Outline each Plasmodium malariae-infected red blood cell.
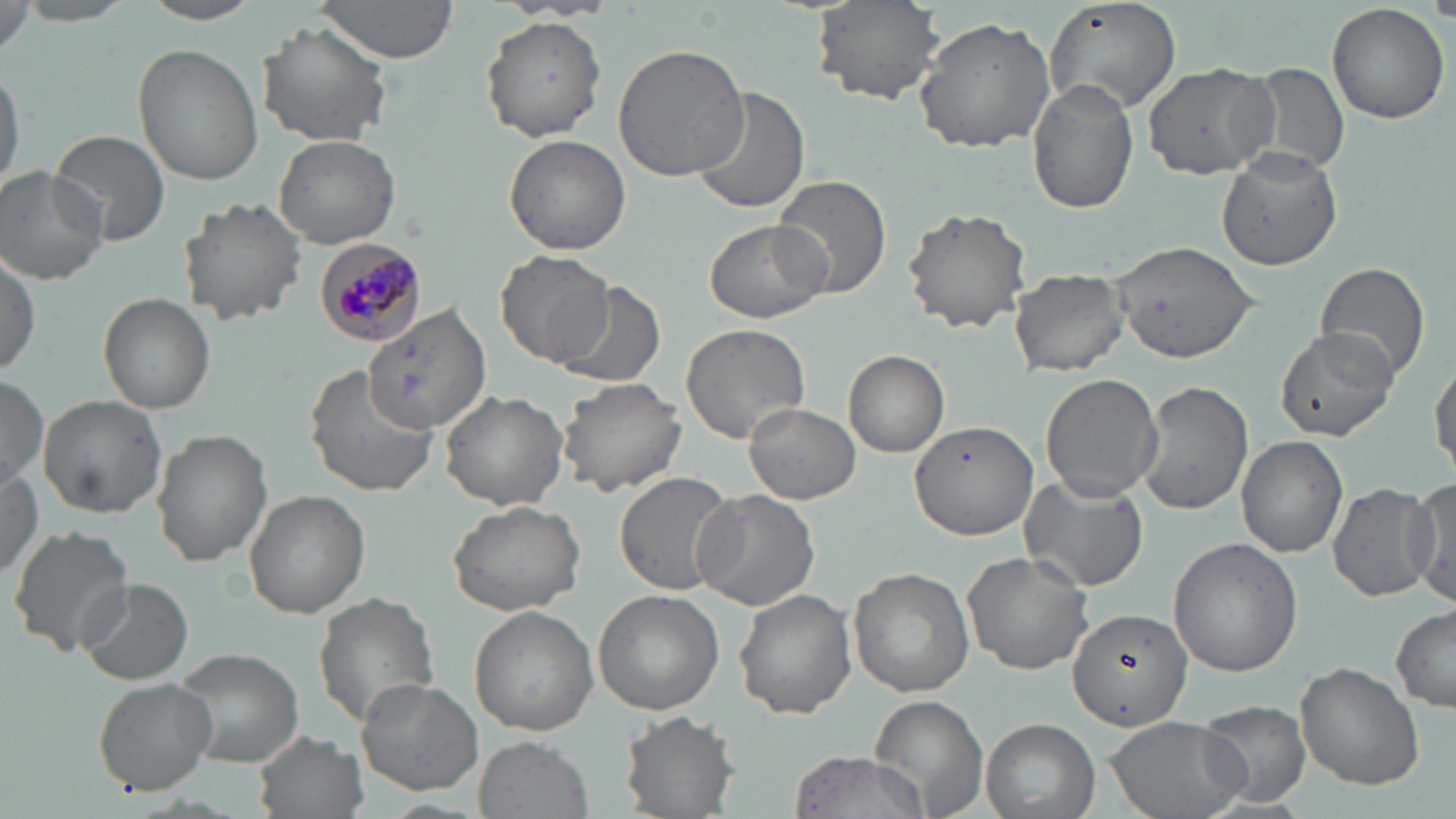

Approximate bounding boxes as named x1/y1/x2/y2 corners in pixels.
Plasmodium malariae-infected red blood cells: (x1=314, y1=239, x2=425, y2=348).

slide-level diagnosis = Plasmodium malariae
magnification = 1000x
image size = 1456×819 pixels
stain = May-Grünwald-Giemsa
preparation = thin blood film
field of view = one of a larger specimen
modality = optical microscopy
uninfected red blood cell locations = approximate bounding boxes as named x1/y1/x2/y2 corners in pixels: (x1=314, y1=0, x2=460, y2=64), (x1=810, y1=0, x2=946, y2=107), (x1=1045, y1=0, x2=1182, y2=115), (x1=136, y1=1, x2=266, y2=25), (x1=1326, y1=4, x2=1450, y2=125), (x1=480, y1=16, x2=607, y2=140), (x1=913, y1=16, x2=1058, y2=153), (x1=257, y1=21, x2=392, y2=147), (x1=613, y1=43, x2=754, y2=182), (x1=132, y1=44, x2=263, y2=185), (x1=0, y1=60, x2=24, y2=198), (x1=1142, y1=63, x2=1280, y2=181), (x1=1248, y1=63, x2=1350, y2=177), (x1=1028, y1=77, x2=1139, y2=214), (x1=688, y1=87, x2=811, y2=217), (x1=49, y1=129, x2=172, y2=244), (x1=274, y1=134, x2=401, y2=249), (x1=504, y1=135, x2=631, y2=255), (x1=1216, y1=147, x2=1345, y2=273), (x1=0, y1=167, x2=110, y2=286), (x1=773, y1=175, x2=893, y2=299), (x1=179, y1=198, x2=307, y2=324), (x1=901, y1=207, x2=1034, y2=333), (x1=703, y1=218, x2=834, y2=324), (x1=1114, y1=240, x2=1258, y2=362), (x1=1, y1=249, x2=42, y2=377), (x1=498, y1=250, x2=616, y2=369), (x1=1315, y1=261, x2=1431, y2=383), (x1=1008, y1=267, x2=1130, y2=377), (x1=553, y1=281, x2=669, y2=389), (x1=99, y1=292, x2=214, y2=414), (x1=362, y1=299, x2=492, y2=438), (x1=681, y1=322, x2=812, y2=443), (x1=1274, y1=327, x2=1396, y2=440), (x1=844, y1=351, x2=950, y2=457), (x1=1431, y1=351, x2=1456, y2=482), (x1=303, y1=366, x2=443, y2=500), (x1=1040, y1=373, x2=1163, y2=503), (x1=0, y1=375, x2=48, y2=487), (x1=555, y1=377, x2=687, y2=498), (x1=1136, y1=381, x2=1253, y2=515), (x1=440, y1=388, x2=569, y2=511), (x1=38, y1=394, x2=166, y2=518), (x1=744, y1=403, x2=860, y2=505), (x1=909, y1=421, x2=1036, y2=540), (x1=151, y1=427, x2=271, y2=565), (x1=1237, y1=435, x2=1348, y2=557), (x1=0, y1=463, x2=46, y2=582), (x1=613, y1=471, x2=736, y2=597), (x1=1018, y1=473, x2=1151, y2=591), (x1=1405, y1=479, x2=1456, y2=606), (x1=1327, y1=481, x2=1442, y2=603), (x1=690, y1=488, x2=819, y2=611), (x1=244, y1=489, x2=369, y2=617), (x1=446, y1=498, x2=587, y2=617), (x1=7, y1=526, x2=133, y2=657), (x1=1167, y1=536, x2=1303, y2=676), (x1=962, y1=551, x2=1098, y2=677), (x1=848, y1=568, x2=974, y2=697), (x1=77, y1=578, x2=194, y2=685), (x1=734, y1=588, x2=856, y2=718), (x1=311, y1=590, x2=442, y2=730), (x1=594, y1=591, x2=724, y2=715), (x1=1391, y1=605, x2=1456, y2=713), (x1=1066, y1=606, x2=1193, y2=732), (x1=470, y1=607, x2=597, y2=734), (x1=173, y1=648, x2=305, y2=768), (x1=1296, y1=662, x2=1425, y2=790), (x1=355, y1=678, x2=483, y2=796), (x1=92, y1=679, x2=216, y2=794), (x1=869, y1=695, x2=990, y2=817), (x1=1198, y1=698, x2=1312, y2=806), (x1=621, y1=709, x2=739, y2=817), (x1=1103, y1=714, x2=1250, y2=819), (x1=981, y1=718, x2=1101, y2=819), (x1=255, y1=730, x2=368, y2=819), (x1=477, y1=735, x2=592, y2=818), (x1=789, y1=750, x2=928, y2=819)